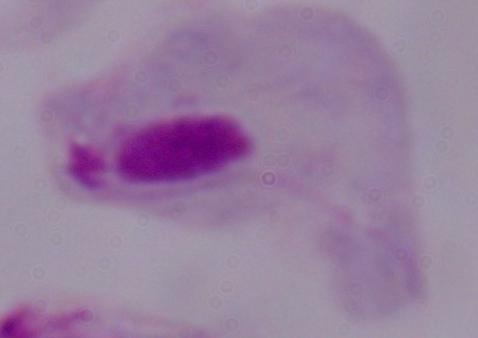

modality: photomicrograph
magnification: 1000x
identification: trichomonad